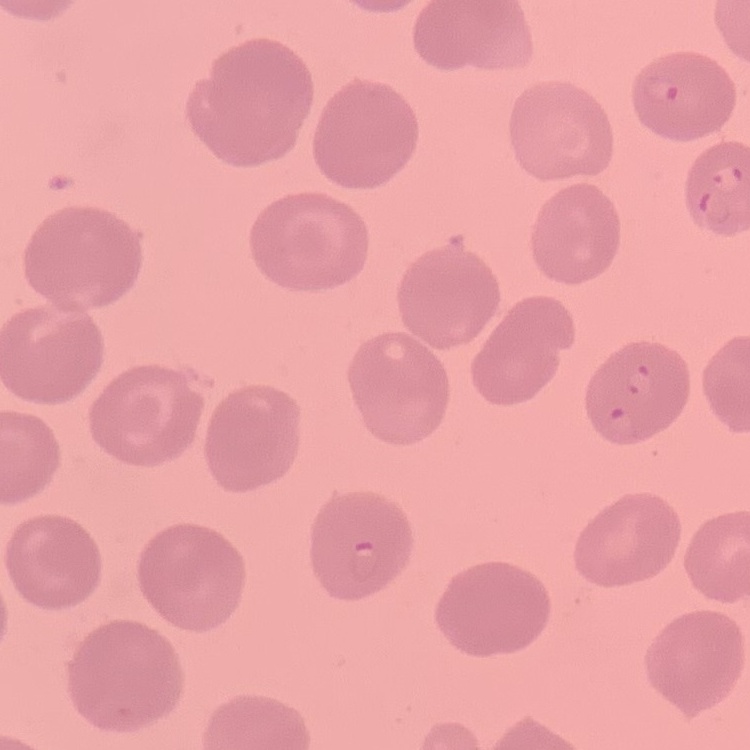
red blood cell morphology = no rouleaux formation
preparation = thin peripheral smear
stain = Field's or Giemsa
image type = square crop of a larger photomicrograph